Report the malaria status of this cell.
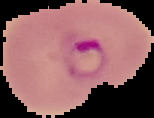

Parasitized.

Summary:
  - Image type: cell region segmented out of the field of view; surrounding area masked to black
  - Image size: 154×118 pixels
  - Preparation: thin blood smear